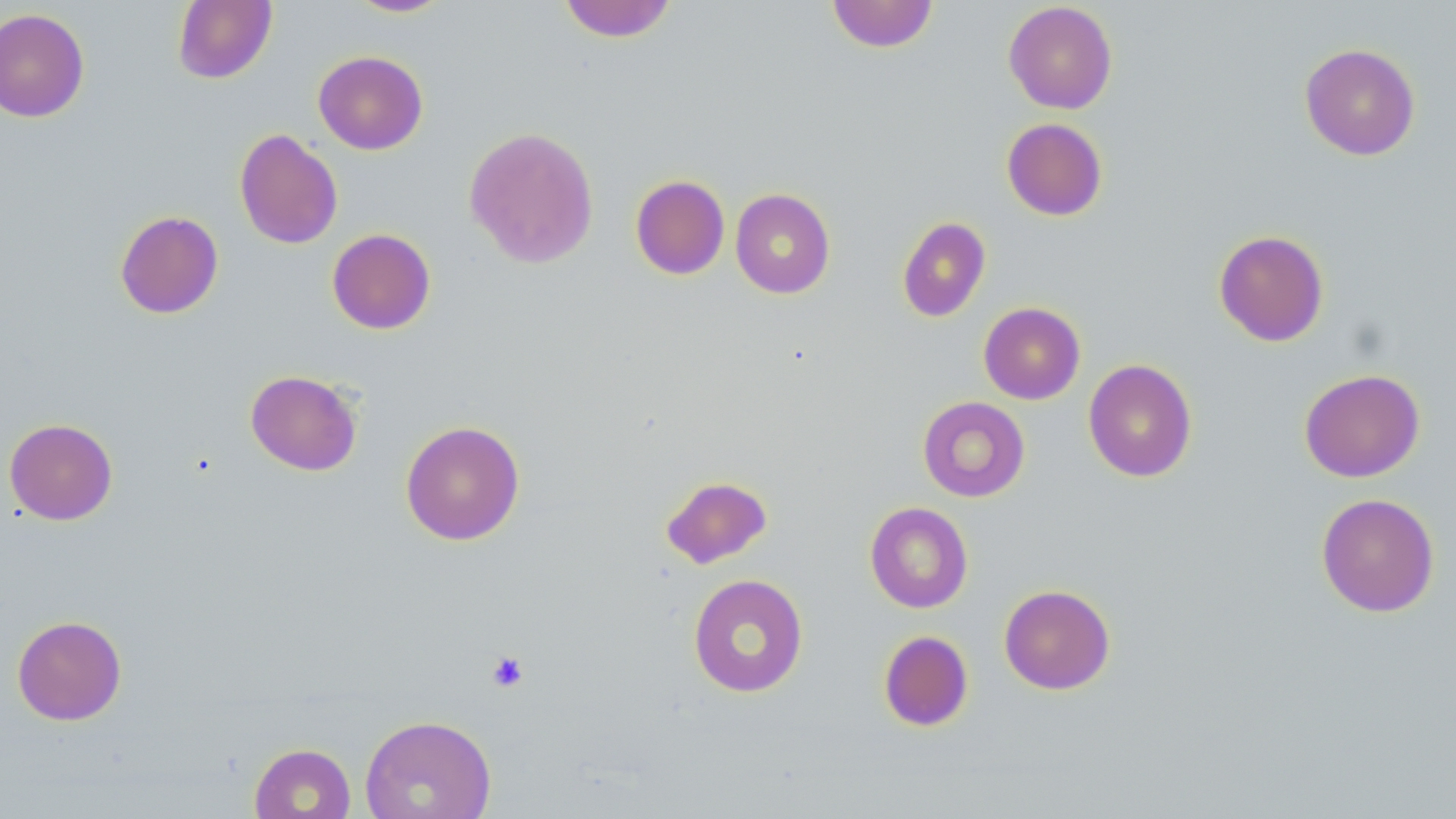
Summary:
  - Coordinate format: approximate bounding boxes as [x1, y1, x2, y2] in pixels
  - Uninfected red blood cell locations: [346, 0, 452, 17], [558, 0, 678, 42], [826, 0, 939, 53], [172, 1, 277, 84], [1003, 2, 1118, 114], [0, 8, 90, 123], [1299, 43, 1421, 161], [313, 50, 428, 155], [1001, 117, 1108, 220], [463, 126, 599, 269], [234, 128, 343, 249], [630, 175, 730, 280], [730, 188, 835, 299], [114, 210, 224, 319], [896, 216, 991, 323], [327, 228, 436, 334], [1213, 229, 1329, 347], [978, 302, 1085, 404], [1083, 358, 1197, 482], [1298, 368, 1425, 482], [245, 369, 362, 476], [917, 396, 1030, 502], [4, 418, 118, 525], [400, 420, 525, 545], [660, 474, 773, 569], [1315, 493, 1440, 617], [865, 502, 973, 613], [687, 573, 809, 697], [998, 584, 1115, 695], [12, 615, 127, 725], [878, 630, 974, 732], [360, 714, 497, 818], [249, 742, 356, 819]
  - Platelet locations: [486, 651, 530, 692]
  - Slide-level diagnosis: no evidence of blood parasites
  - Modality: optical microscopy
  - Stain: May-Grünwald-Giemsa
  - Field of view: single
  - Preparation: thin blood smear
  - Magnification: 1000x
  - Image size: 1456×819 pixels